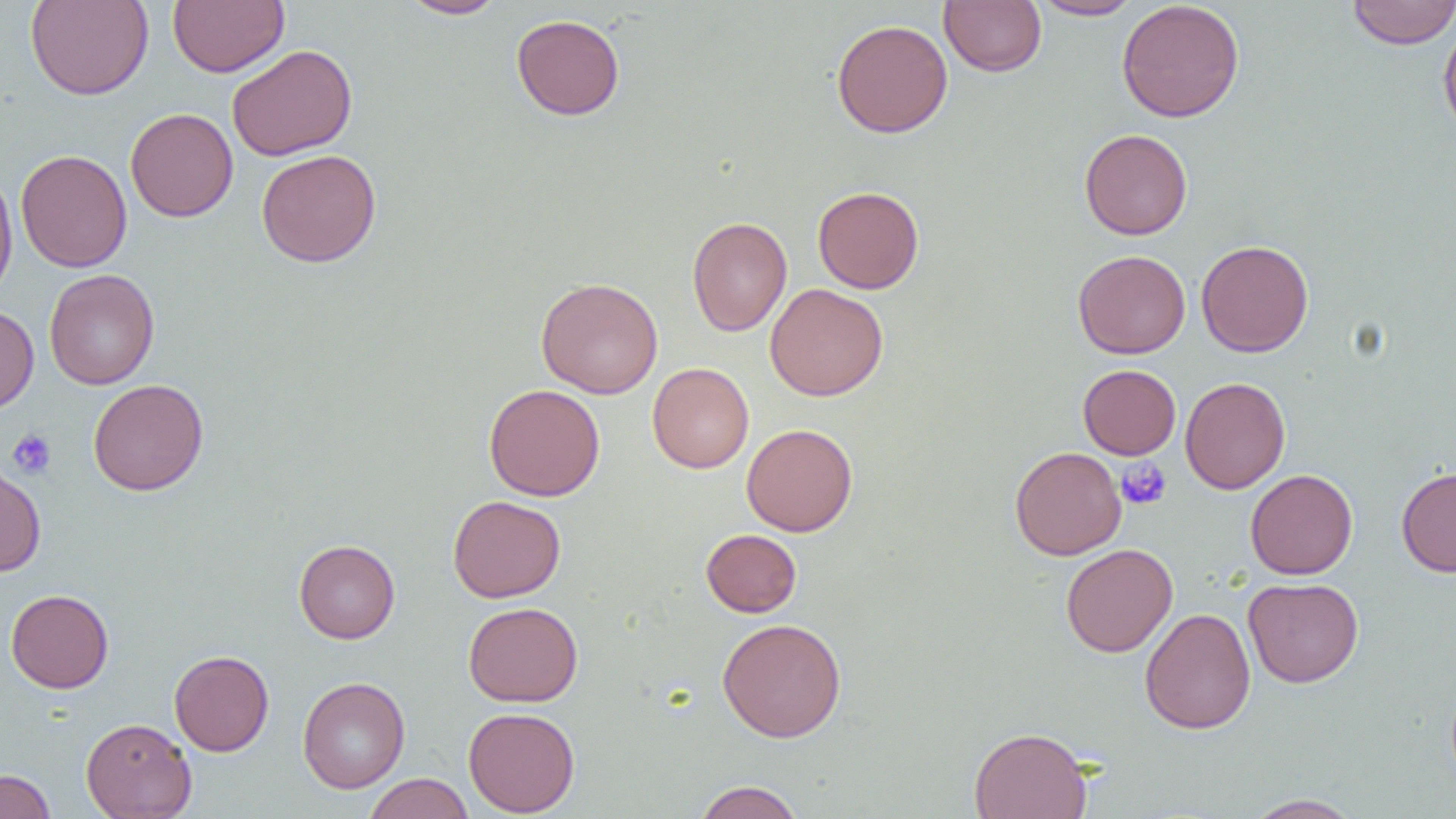

slide-level diagnosis = negative for blood parasites
uninfected red blood cell locations = approximate bounding boxes as named x1/y1/x2/y2 corners in pixels: (x1=24, y1=0, x2=154, y2=100), (x1=167, y1=0, x2=289, y2=77), (x1=399, y1=0, x2=506, y2=19), (x1=939, y1=0, x2=1046, y2=77), (x1=1030, y1=0, x2=1141, y2=20), (x1=1116, y1=0, x2=1245, y2=123), (x1=1347, y1=1, x2=1456, y2=48), (x1=511, y1=14, x2=625, y2=120), (x1=831, y1=19, x2=953, y2=139), (x1=1438, y1=19, x2=1456, y2=139), (x1=227, y1=44, x2=357, y2=161), (x1=125, y1=107, x2=238, y2=222), (x1=1079, y1=128, x2=1193, y2=240), (x1=16, y1=149, x2=132, y2=272), (x1=256, y1=149, x2=381, y2=267), (x1=0, y1=165, x2=18, y2=304), (x1=813, y1=186, x2=924, y2=294), (x1=687, y1=216, x2=792, y2=336), (x1=1196, y1=240, x2=1313, y2=357), (x1=1073, y1=250, x2=1190, y2=359), (x1=44, y1=269, x2=159, y2=389), (x1=536, y1=277, x2=664, y2=399), (x1=765, y1=283, x2=889, y2=401), (x1=0, y1=305, x2=38, y2=414), (x1=647, y1=363, x2=754, y2=473), (x1=1078, y1=365, x2=1180, y2=459), (x1=1180, y1=377, x2=1290, y2=494), (x1=88, y1=378, x2=209, y2=496), (x1=484, y1=384, x2=605, y2=501), (x1=742, y1=424, x2=857, y2=536), (x1=1009, y1=446, x2=1126, y2=560), (x1=0, y1=463, x2=46, y2=577), (x1=1396, y1=466, x2=1456, y2=577), (x1=1245, y1=469, x2=1358, y2=580), (x1=447, y1=495, x2=566, y2=603), (x1=701, y1=529, x2=801, y2=617), (x1=294, y1=539, x2=400, y2=643), (x1=1060, y1=543, x2=1178, y2=658), (x1=1243, y1=577, x2=1364, y2=688), (x1=5, y1=589, x2=114, y2=693), (x1=462, y1=601, x2=583, y2=706), (x1=1140, y1=607, x2=1256, y2=734), (x1=717, y1=618, x2=847, y2=742), (x1=169, y1=650, x2=274, y2=756), (x1=297, y1=676, x2=410, y2=794), (x1=463, y1=707, x2=580, y2=816), (x1=81, y1=717, x2=196, y2=819), (x1=969, y1=726, x2=1093, y2=819), (x1=0, y1=769, x2=56, y2=819), (x1=362, y1=773, x2=474, y2=819), (x1=691, y1=780, x2=806, y2=819), (x1=1242, y1=794, x2=1364, y2=818)
modality = optical microscopy
field of view = one of a larger specimen
image size = 1456×819 pixels
platelet locations = approximate bounding boxes as named x1/y1/x2/y2 corners in pixels: (x1=7, y1=429, x2=57, y2=479), (x1=1115, y1=457, x2=1171, y2=510)
preparation = thin blood smear
magnification = 1000x